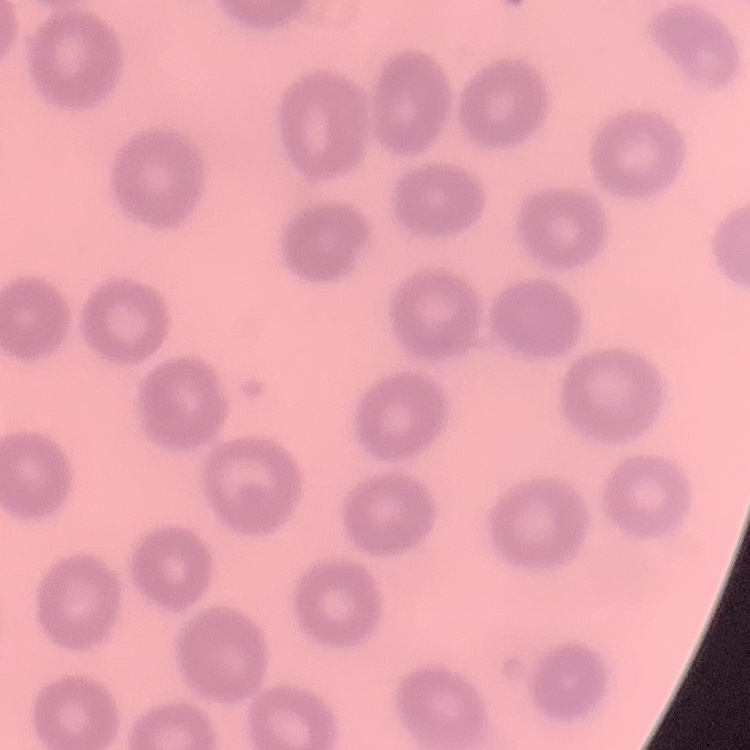

Summary:
  - Erythrocyte morphology: no rouleaux formation
  - Preparation: thin blood film
  - Stain: Field's or Giemsa
  - Image type: one tile cut from a larger photomicrograph